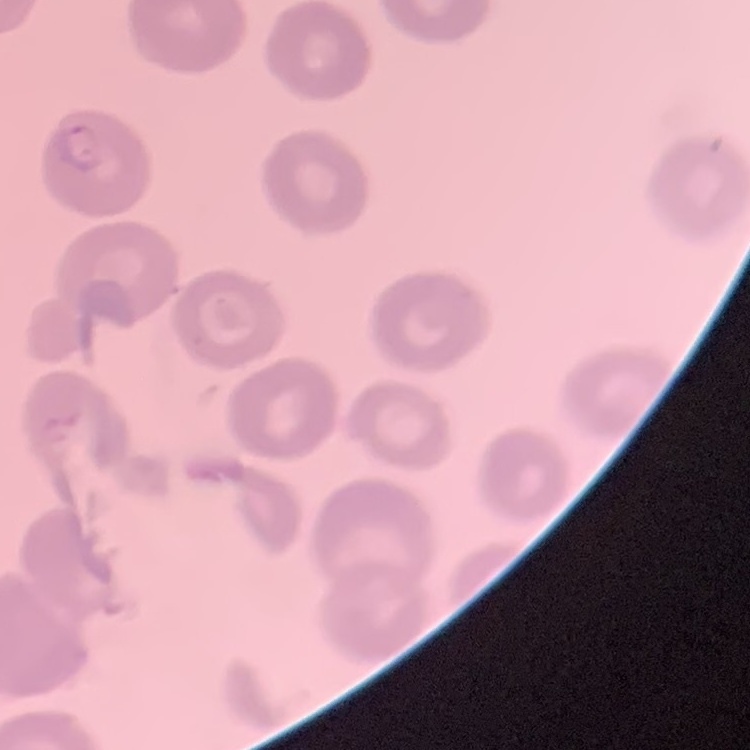
red blood cell morphology = no rouleaux formation
stain = Field's or Giemsa
preparation = thin blood film
image type = square crop of a larger photomicrograph